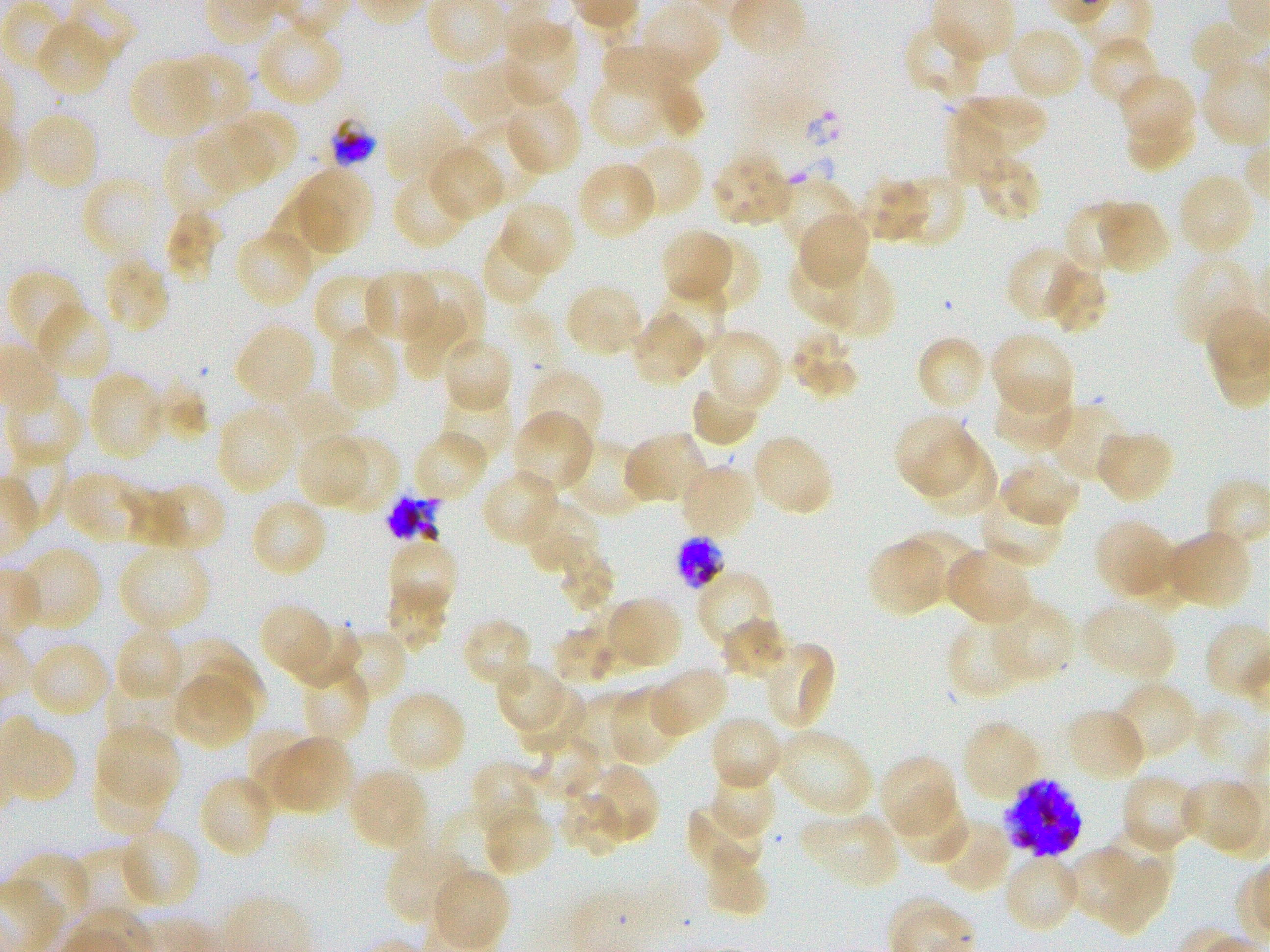

Not every red blood cell is marked. A life-cycle stage — or a range of stages, where the recorded stages span more than one — follows each staged infected red blood cell.
locations of infected red blood cells = approximate bounding boxes as {x1, y1, x2, y2} in pixels: {675, 536, 727, 590} late trophozoite to early schizont; {1005, 777, 1083, 859} late trophozoite to late schizont
objective = 100x, oil immersion, numerical aperture 1.25
preparation = thin blood smear
locations of red blood cells of indeterminate infection status = approximate bounding boxes as {x1, y1, x2, y2} in pixels: {330, 118, 377, 167}, {385, 492, 443, 544}
stain = Giemsa
donor blood group = O+
culture = static in-vitro Plasmodium falciparum strain 3D7
field of view = one from this slide
locations of uninfected red blood cells = approximate bounding boxes as {x1, y1, x2, y2} in pixels: {639, 3, 722, 85}, {34, 19, 113, 97}, {502, 21, 579, 106}, {904, 21, 986, 103}, {256, 22, 344, 107}, {1189, 22, 1258, 82}, {1007, 25, 1085, 101}, {1087, 34, 1162, 108}, {600, 40, 679, 97}, {173, 53, 251, 130}, {128, 59, 213, 140}, {443, 61, 547, 128}, {588, 72, 674, 147}, {1119, 74, 1195, 146}, {653, 79, 705, 141}, {958, 94, 1047, 161}, {503, 95, 583, 175}, {383, 103, 468, 186}, {943, 106, 1033, 184}, {225, 108, 299, 180}, {24, 109, 100, 191}, {1126, 112, 1195, 174}, {464, 121, 536, 201}, {196, 122, 271, 194}, {161, 137, 236, 219}, {624, 142, 705, 218}, {427, 145, 504, 221}, {710, 152, 792, 228}, {976, 154, 1043, 223}, {575, 161, 657, 241}, {293, 167, 374, 252}, {391, 171, 471, 250}, {1177, 171, 1255, 257}, {891, 174, 968, 248}, {82, 176, 165, 263}, {858, 176, 928, 244}, {776, 178, 857, 258}, {266, 195, 350, 275}, {498, 201, 575, 278}, {1097, 201, 1169, 274}, {1061, 203, 1133, 275}, {163, 209, 225, 283}, {798, 212, 871, 290}, {234, 227, 314, 309}, {660, 228, 733, 304}, {480, 229, 551, 308}, {696, 238, 761, 314}, {1005, 245, 1082, 322}, {1173, 255, 1256, 348}, {789, 257, 866, 329}, {101, 258, 171, 335}, {815, 260, 895, 338}, {1043, 262, 1108, 334}, {409, 267, 485, 348}, {6, 268, 86, 354}, {362, 269, 438, 343}, {314, 272, 388, 350}, {652, 282, 726, 357}, {565, 284, 642, 358}, {402, 298, 469, 379}, {36, 303, 114, 381}, {630, 310, 707, 386}, {234, 322, 316, 405}, {328, 326, 400, 415}, {706, 329, 784, 412}, {790, 329, 861, 401}, {989, 333, 1074, 414}, {442, 335, 514, 413}, {915, 335, 987, 411}, {526, 369, 605, 451}, {87, 370, 166, 461}, {992, 381, 1073, 451}, {149, 382, 208, 444}, {690, 383, 759, 448}, {276, 389, 355, 455}, {5, 390, 86, 467}, {439, 391, 513, 464}, {1042, 403, 1128, 484}, {216, 405, 298, 494}, {511, 411, 594, 492}, {893, 413, 975, 496}, {1095, 428, 1174, 504}, {412, 430, 488, 502}, {623, 431, 709, 506}, {750, 433, 834, 517}, {298, 434, 370, 511}, {332, 435, 397, 515}, {562, 437, 653, 519}, {917, 438, 997, 517}, {1001, 459, 1082, 526}, {680, 463, 758, 538}, {481, 468, 561, 547}, {63, 470, 145, 545}, {150, 482, 226, 554}, {977, 487, 1067, 568}, {125, 490, 185, 548}, {250, 497, 329, 577}, {521, 499, 601, 576}, {1094, 518, 1174, 598}, {902, 528, 979, 602}, {1166, 528, 1251, 610}, {386, 537, 459, 614}, {865, 538, 946, 617}, {16, 546, 103, 633}, {118, 547, 211, 633}, {557, 548, 615, 615}, {945, 548, 1033, 627}, {697, 571, 775, 650}, {385, 583, 449, 654}, {605, 595, 683, 670}, {992, 598, 1075, 682}, {583, 600, 656, 673}, {1080, 601, 1176, 681}, {259, 604, 335, 681}, {461, 618, 535, 690}, {720, 618, 790, 681}, {946, 619, 1029, 699}, {290, 620, 360, 688}, {551, 624, 624, 684}, {114, 626, 185, 702}, {336, 627, 407, 703}, {174, 637, 261, 717}, {27, 640, 112, 718}, {762, 641, 837, 731}, {192, 659, 269, 731}, {495, 663, 575, 739}, {299, 664, 370, 745}, {648, 666, 729, 737}, {172, 672, 254, 750}, {1111, 680, 1197, 761}, {105, 682, 180, 743}, {515, 683, 587, 753}, {607, 687, 688, 767}, {385, 690, 468, 774}, {565, 694, 641, 765}, {1064, 707, 1147, 784}, {709, 716, 782, 793}, {961, 719, 1040, 802}, {97, 723, 181, 805}, {246, 727, 314, 795}, {776, 728, 874, 817}, {526, 735, 601, 805}, {270, 736, 352, 813}, {879, 754, 958, 835}, {470, 761, 544, 833}, {588, 763, 659, 844}, {91, 765, 171, 837}, {710, 765, 774, 840}, {347, 766, 429, 850}, {1120, 772, 1199, 852}, {197, 773, 275, 859}, {1179, 777, 1265, 856}, {558, 787, 628, 856}, {895, 795, 970, 866}, {684, 802, 768, 875}, {481, 804, 554, 879}, {799, 810, 899, 890}, {937, 819, 1013, 893}, {119, 826, 202, 909}, {1099, 827, 1177, 908}, {383, 842, 471, 925}, {1065, 848, 1147, 926}, {1094, 849, 1170, 936}, {704, 850, 769, 918}, {1002, 852, 1082, 933}, {429, 868, 509, 949}
image size = 1270×952 pixels